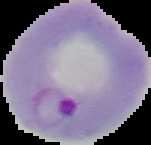
Summary:
  - Malaria status: parasitized
  - Preparation: thin blood film
  - Image size: 151×145 pixels
  - Image type: segmented cell region with the area outside set to black